Classify this cell by malaria status.
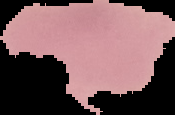

Uninfected.

From a thin blood film. Image is 175×115 pixels. The area outside the segmented cell region is set to black.